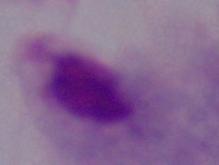
Photomicrograph. Captured at 1000x magnification. A trichomonad is seen.